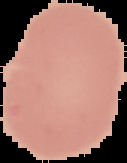

Summary:
  - Malaria status: uninfected
  - Preparation: thin blood smear
  - Image type: segmented cell region with the area outside set to black
  - Image size: 127×163 pixels